Give the position of every Plasmodium parasite visible.
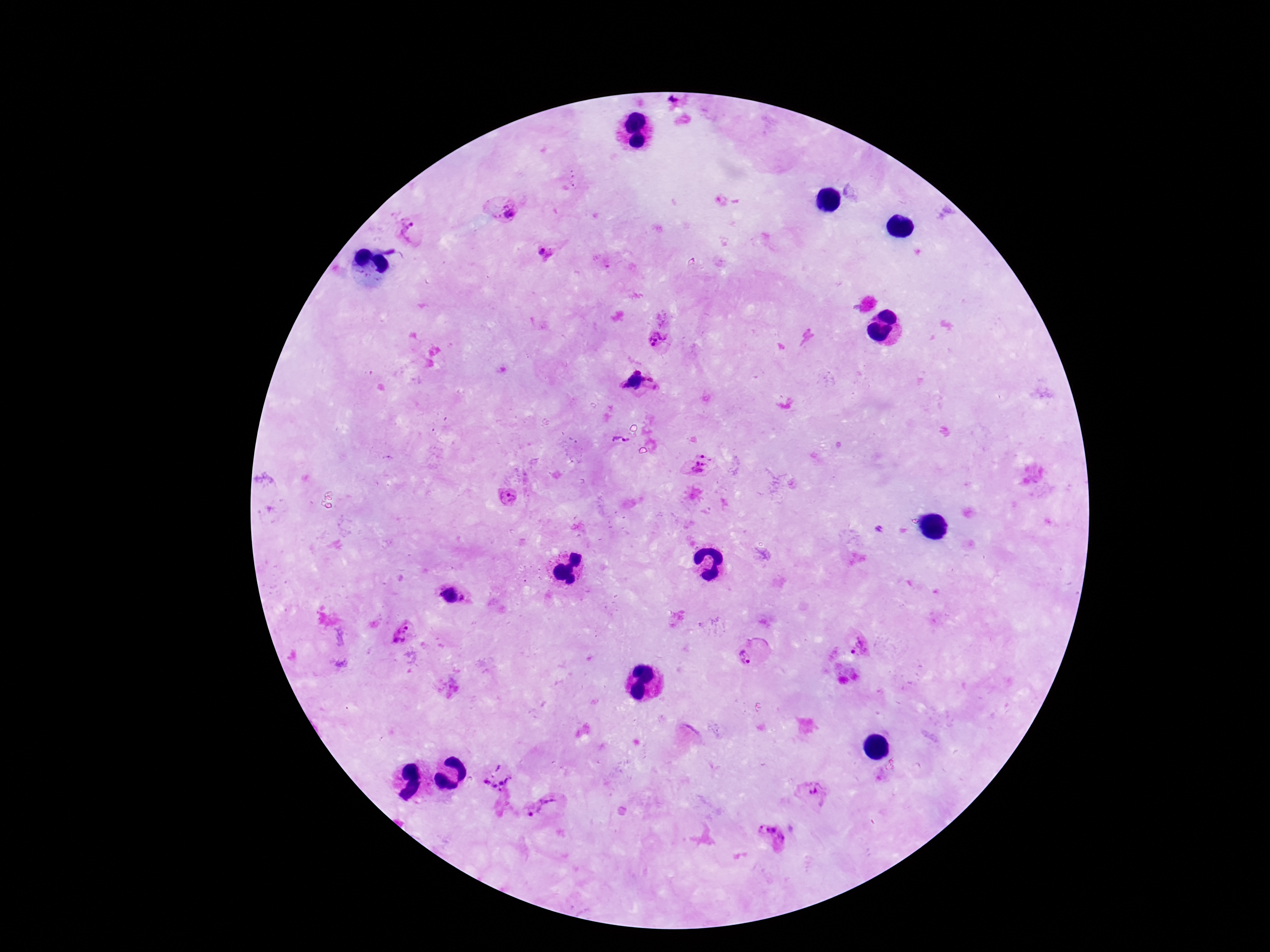

Approximate centers as (x, y) in pixels.
Plasmodium parasites: (507, 212), (411, 230), (543, 253), (660, 341), (638, 372), (650, 380), (635, 381), (626, 385), (615, 438), (627, 439), (708, 454), (698, 463), (704, 465), (696, 471), (508, 497), (449, 593), (402, 632), (861, 645), (748, 652), (497, 774), (815, 789), (542, 809), (771, 835).

Summary:
  - Capture: smartphone camera through the microscope eyepiece
  - Patient malaria status: positive
  - Magnification: 100x
  - Stain: Giemsa
  - Image size: 1270×952 pixels
  - Field of view: single
  - Preparation: thick blood film